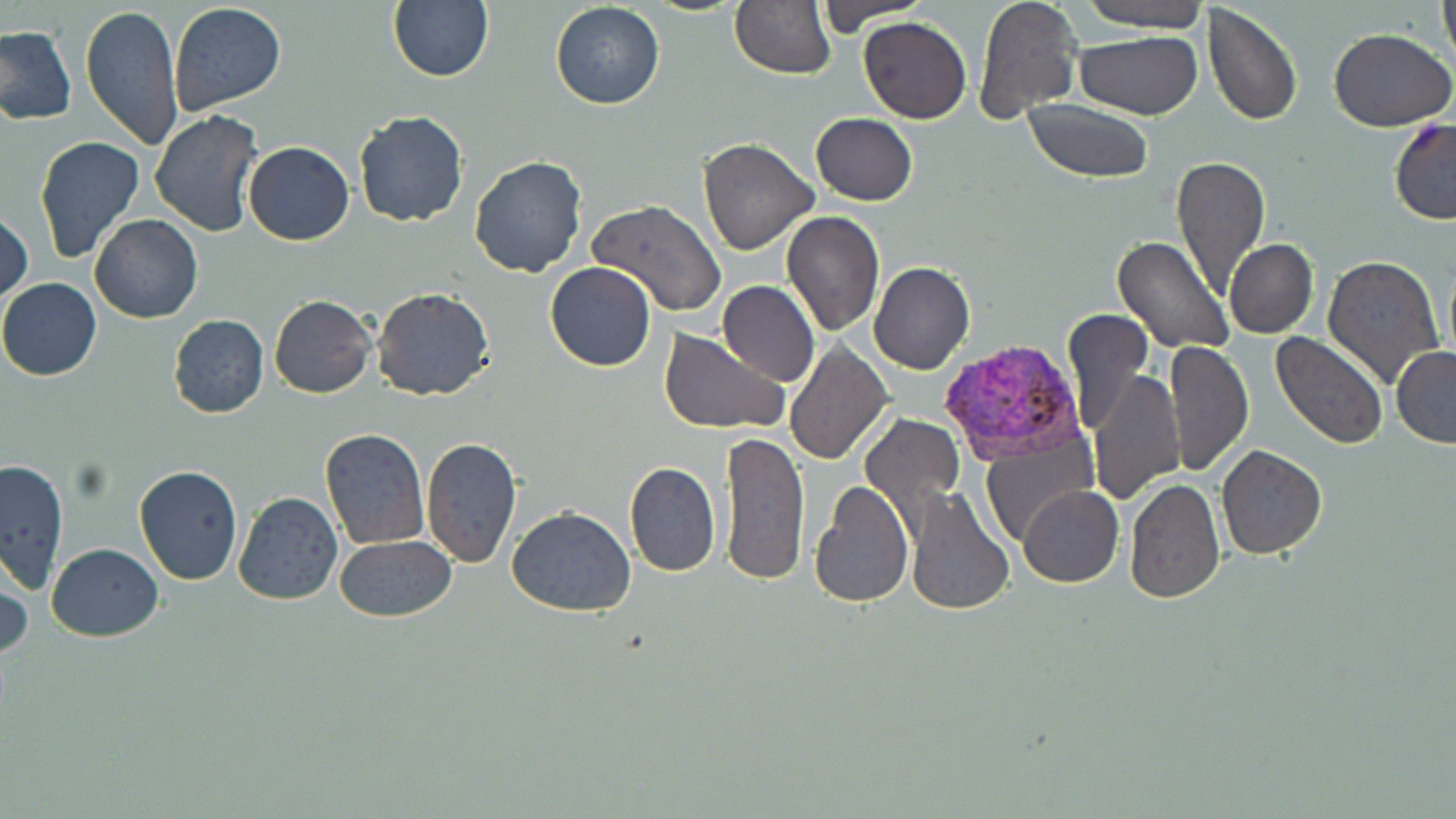
Summary:
  - Coordinate format: approximate bounding boxes as named x1/y1/x2/y2 corners in pixels
  - Plasmodium vivax-infected red blood cell locations: (x1=936, y1=337, x2=1087, y2=463)
  - Uninfected red blood cell locations: (x1=388, y1=0, x2=495, y2=83), (x1=730, y1=0, x2=836, y2=80), (x1=816, y1=0, x2=931, y2=31), (x1=973, y1=0, x2=1082, y2=122), (x1=1076, y1=0, x2=1212, y2=31), (x1=1438, y1=0, x2=1456, y2=68), (x1=550, y1=1, x2=665, y2=110), (x1=80, y1=2, x2=184, y2=151), (x1=167, y1=2, x2=287, y2=116), (x1=1202, y1=4, x2=1304, y2=127), (x1=859, y1=16, x2=971, y2=123), (x1=0, y1=26, x2=75, y2=125), (x1=1329, y1=28, x2=1455, y2=129), (x1=1075, y1=29, x2=1202, y2=120), (x1=1024, y1=99, x2=1154, y2=184), (x1=149, y1=110, x2=264, y2=237), (x1=353, y1=111, x2=469, y2=226), (x1=811, y1=113, x2=917, y2=205), (x1=1389, y1=119, x2=1456, y2=225), (x1=35, y1=136, x2=145, y2=263), (x1=698, y1=138, x2=818, y2=256), (x1=244, y1=141, x2=355, y2=246), (x1=469, y1=154, x2=589, y2=279), (x1=1171, y1=157, x2=1270, y2=296), (x1=589, y1=199, x2=727, y2=317), (x1=0, y1=207, x2=33, y2=309), (x1=780, y1=209, x2=883, y2=335), (x1=89, y1=213, x2=203, y2=323), (x1=1111, y1=236, x2=1234, y2=354), (x1=1225, y1=238, x2=1318, y2=339), (x1=1322, y1=254, x2=1446, y2=390), (x1=545, y1=261, x2=657, y2=372), (x1=869, y1=261, x2=974, y2=374), (x1=0, y1=278, x2=102, y2=380), (x1=718, y1=281, x2=819, y2=385), (x1=371, y1=286, x2=495, y2=401), (x1=270, y1=295, x2=376, y2=399), (x1=1062, y1=308, x2=1152, y2=437), (x1=168, y1=314, x2=270, y2=419), (x1=659, y1=328, x2=786, y2=434), (x1=1271, y1=331, x2=1389, y2=451), (x1=1167, y1=338, x2=1253, y2=475), (x1=785, y1=339, x2=893, y2=464), (x1=1391, y1=345, x2=1456, y2=447), (x1=1090, y1=368, x2=1184, y2=506), (x1=862, y1=414, x2=964, y2=525), (x1=320, y1=428, x2=429, y2=550), (x1=721, y1=429, x2=810, y2=585), (x1=420, y1=435, x2=523, y2=569), (x1=983, y1=442, x2=1094, y2=548), (x1=1216, y1=446, x2=1326, y2=559), (x1=0, y1=458, x2=69, y2=594), (x1=624, y1=461, x2=720, y2=576), (x1=134, y1=465, x2=243, y2=585), (x1=1123, y1=479, x2=1223, y2=603), (x1=809, y1=481, x2=913, y2=607), (x1=1019, y1=485, x2=1123, y2=588), (x1=905, y1=486, x2=1014, y2=616), (x1=232, y1=491, x2=342, y2=605), (x1=506, y1=506, x2=636, y2=616), (x1=333, y1=536, x2=457, y2=622), (x1=47, y1=543, x2=163, y2=641), (x1=0, y1=558, x2=32, y2=668)
  - Slide-level diagnosis: Plasmodium vivax
  - Field of view: single
  - Preparation: thin blood film
  - Magnification: 1000x
  - Modality: optical microscopy
  - Image size: 1456×819 pixels
  - Stain: May-Grünwald-Giemsa